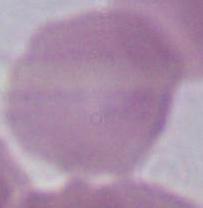
Summary:
  - Modality: photomicrograph
  - Identification: erythrocyte
  - Magnification: 1000x